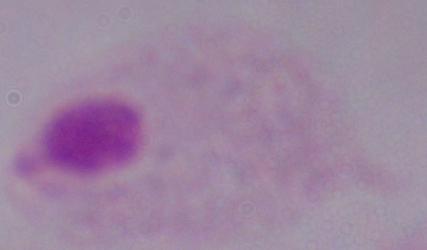

Photomicrograph. A trichomonad is shown. Captured at 1000x magnification.